State the preparation type.
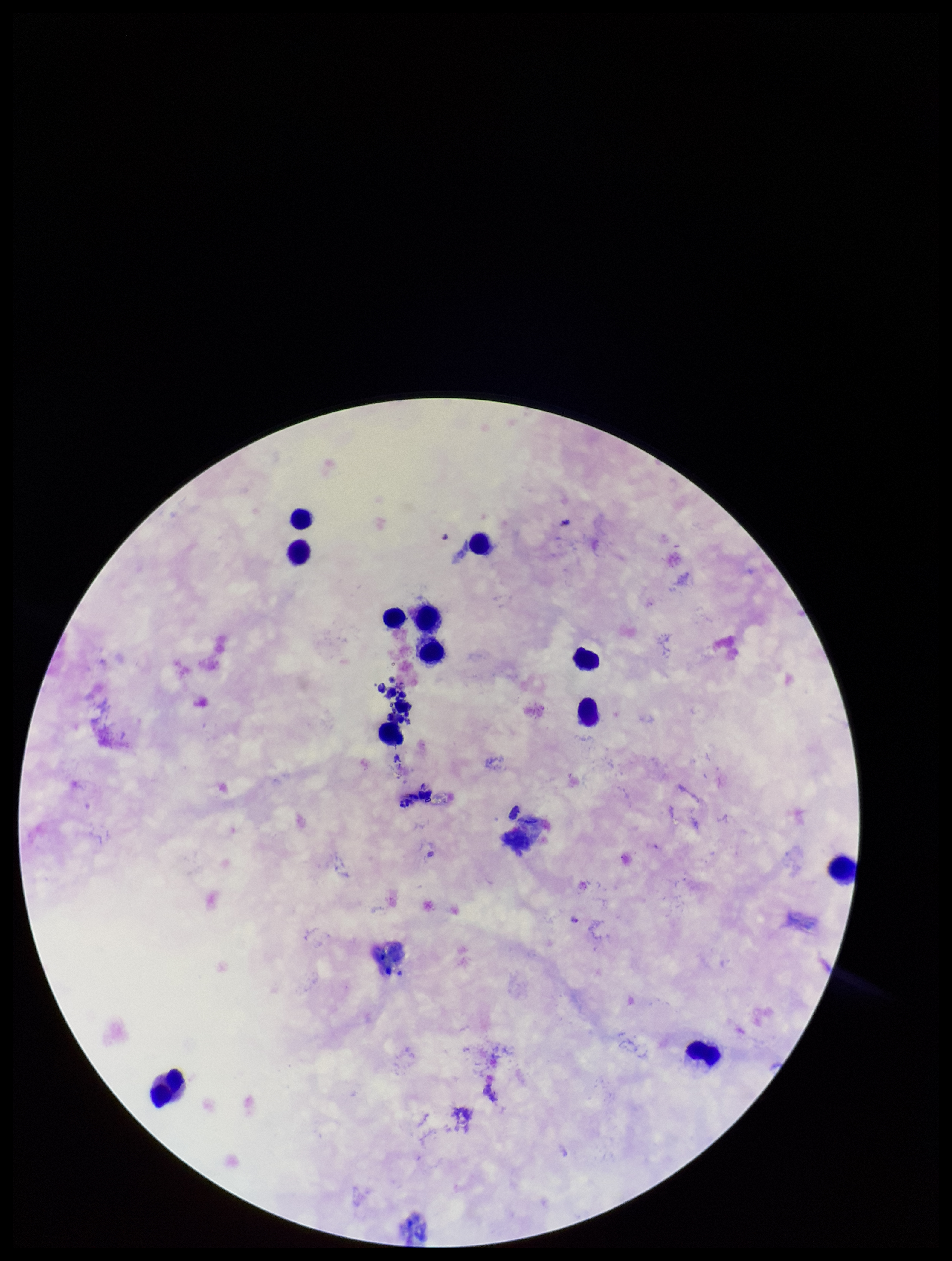

A thick smear.

Summary:
  - Leukocyte count: 12
  - Plasmodium parasites: identified
  - Parasite count: 1
  - Field of view: single
  - Patient malaria status: positive
  - Species reported for this patient: Plasmodium falciparum
  - Stain: Giemsa
  - Image size: 952×1261 pixels
  - Capture: smartphone photograph through the microscope eyepiece